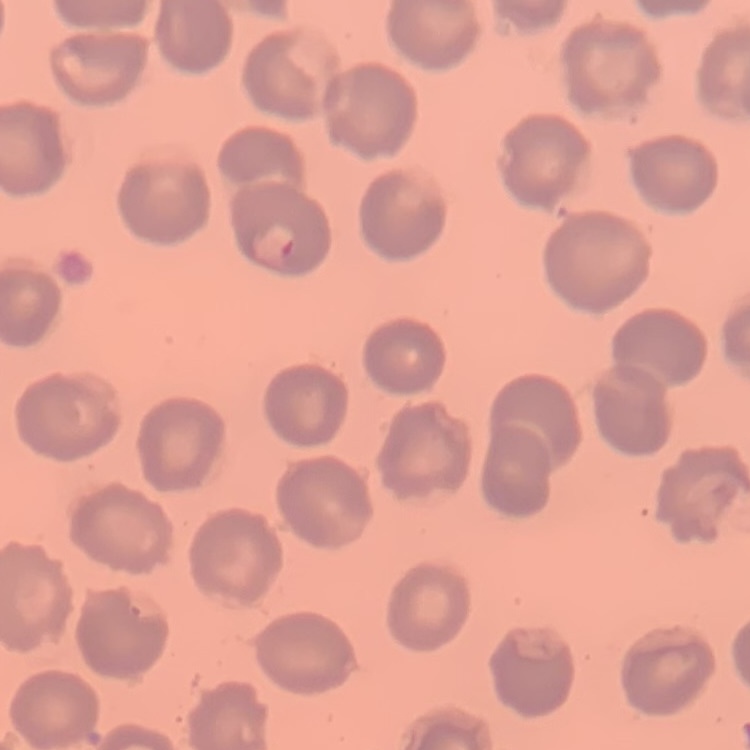

Summary:
  - Erythrocyte morphology: no rouleaux formation
  - Stain: Field's or Giemsa
  - Preparation: thin blood smear
  - Image type: square crop of a larger photomicrograph